Locate every white blood cell.
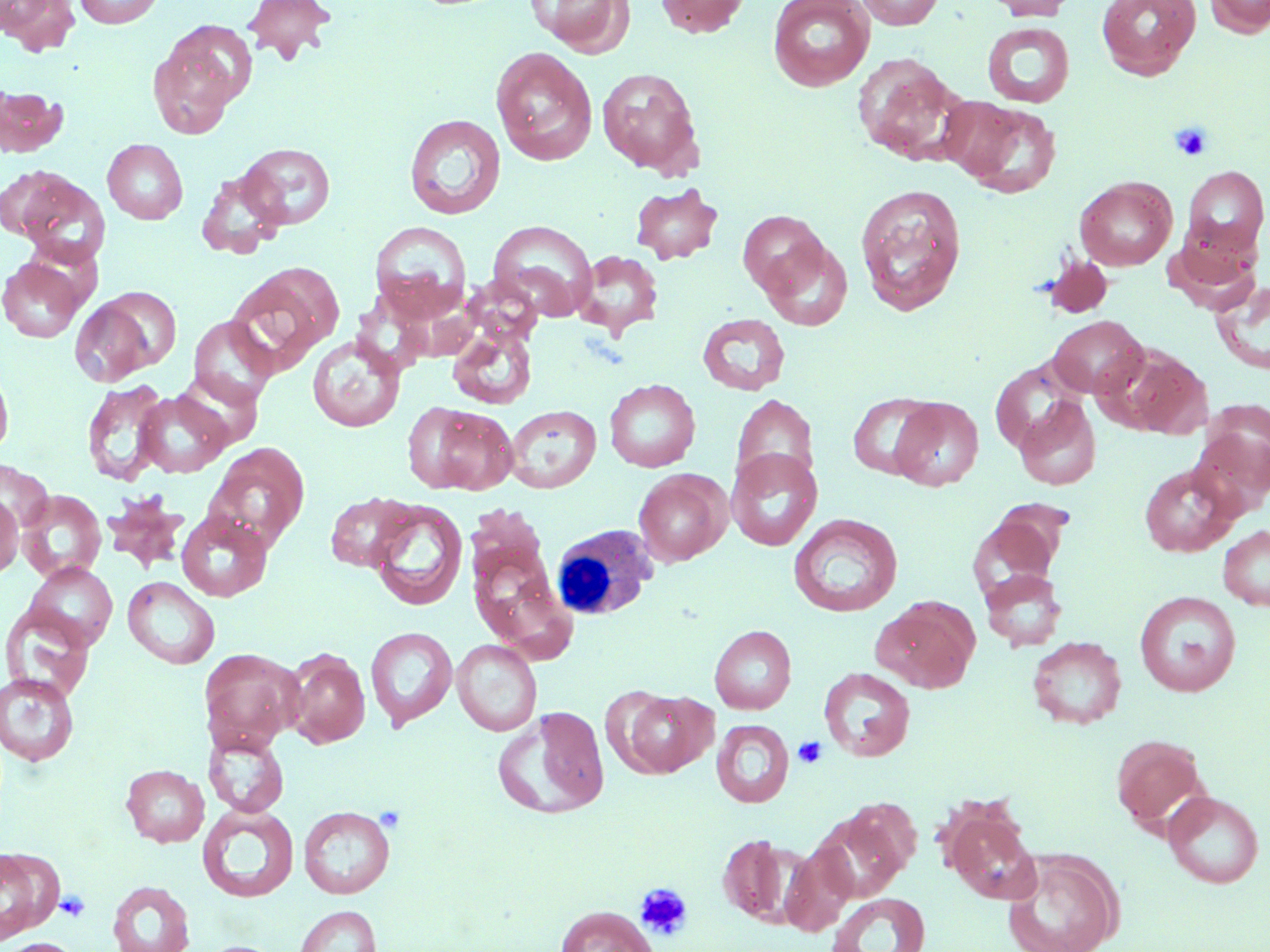

Approximate bounding boxes as (x1,y1)-(x2,y2) corner pairs in pixels.
White blood cells: (552,523)-(669,622).

Summary:
  - Uninfected red blood cell locations: (1,0)-(81,56), (73,0)-(164,28), (243,0)-(336,63), (655,0)-(750,38), (768,0)-(875,91), (855,0)-(945,30), (985,0)-(1077,21), (1097,0)-(1201,80), (1203,0)-(1270,37), (527,1)-(634,54), (982,22)-(1075,107), (147,28)-(249,137), (490,47)-(598,165), (852,53)-(966,165), (597,67)-(703,175), (0,87)-(68,157), (950,98)-(1062,198), (404,114)-(506,220), (102,139)-(188,224), (238,143)-(336,230), (1,165)-(77,241), (1182,166)-(1268,257), (196,169)-(287,259), (18,175)-(110,267), (1074,176)-(1177,270), (630,182)-(723,265), (855,183)-(967,316), (738,210)-(828,297), (489,220)-(597,320), (370,221)-(471,319), (1164,231)-(1259,314), (760,238)-(852,331), (573,250)-(664,339), (0,256)-(86,343), (226,265)-(341,373), (1211,280)-(1270,375), (97,285)-(182,374), (69,299)-(156,387), (697,313)-(790,395), (188,315)-(277,409), (446,315)-(539,413), (1048,315)-(1148,399), (307,334)-(405,433), (1107,344)-(1212,438), (990,360)-(1085,455), (0,363)-(14,460), (172,370)-(264,450), (82,379)-(171,487), (605,379)-(700,472), (134,390)-(232,477), (847,392)-(939,480), (731,393)-(818,490), (890,397)-(984,490), (1014,397)-(1101,491), (1196,400)-(1270,509), (407,403)-(519,495), (504,405)-(602,493), (205,441)-(310,550), (726,449)-(822,551), (0,459)-(54,534), (1138,463)-(1241,557), (633,469)-(730,566), (18,490)-(106,582), (325,491)-(419,572), (102,492)-(190,573), (0,493)-(23,578), (367,499)-(468,611), (973,500)-(1070,588), (176,510)-(273,601), (789,513)-(903,617), (1218,525)-(1270,611), (464,527)-(570,657), (26,563)-(117,650), (980,568)-(1067,651), (122,576)-(220,669), (1134,591)-(1240,697), (870,596)-(979,693), (1,605)-(96,703), (709,625)-(796,714), (365,626)-(458,730), (1027,636)-(1127,729), (451,639)-(542,736), (199,648)-(302,752), (283,649)-(370,748), (819,667)-(915,761), (1,672)-(80,766), (616,689)-(717,778), (494,706)-(609,819), (711,719)-(794,807), (203,731)-(289,817), (1111,734)-(1208,831), (121,764)-(209,847), (1163,790)-(1265,888), (198,804)-(298,902), (818,804)-(915,901), (299,805)-(395,899), (945,809)-(1041,905), (717,834)-(797,926), (781,840)-(857,936), (0,846)-(59,944), (1002,849)-(1122,952), (107,880)-(194,952), (826,892)-(931,952), (294,905)-(382,952), (555,905)-(659,952), (1,938)-(82,952)
  - Platelet locations: (1170,123)-(1213,161), (793,736)-(827,768), (634,883)-(694,941), (54,890)-(90,922)
  - Slide-level diagnosis: no evidence of blood parasites
  - Modality: optical microscopy
  - Stain: May-Grünwald-Giemsa
  - Preparation: thin blood film
  - Image size: 1270×952 pixels
  - Field of view: single
  - Magnification: 1000x